Classify this cell by malaria status.
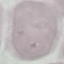
It is uninfected.

Summary:
  - Stain: Giemsa
  - Capture: smartphone camera at the microscope eyepiece
  - Image type: automatically extracted cell patch, resized to 64 × 64 pixels
  - Preparation: thin blood film